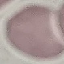
result = no malaria parasites detected
preparation = thin blood smear
image type = cell patch, automatically extracted from a larger field of view and resized to 64 × 64 pixels
stain = Giemsa
capture = smartphone camera at the microscope eyepiece